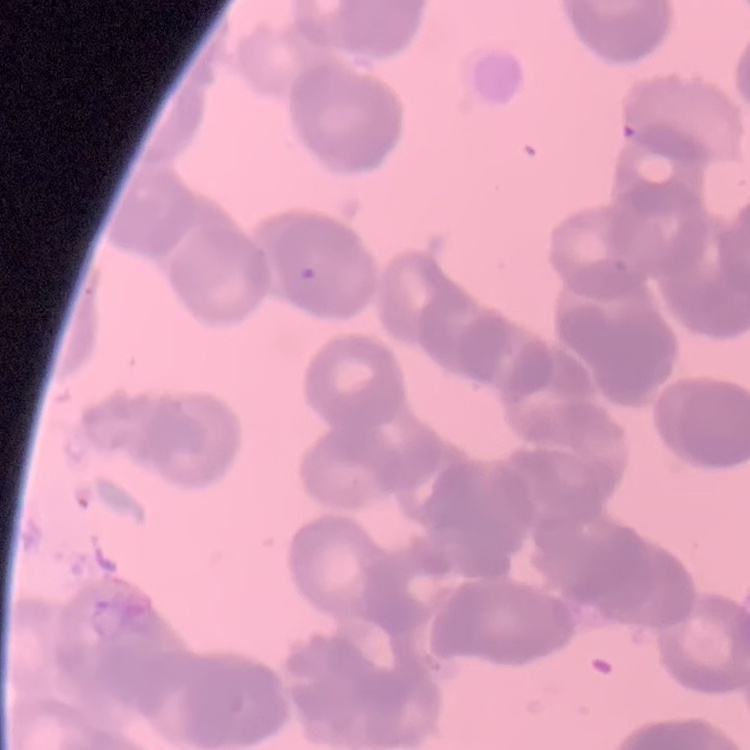
The erythrocytes show rouleaux formation. Thin blood smear. Field's or Giemsa stain. One tile cut from a larger photomicrograph.